Comment on the morphology of the red blood cells.
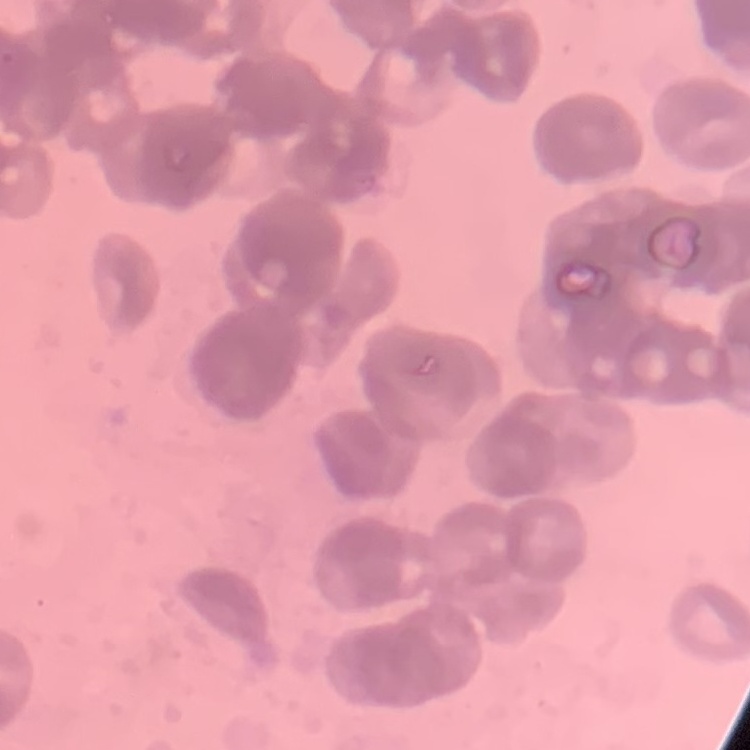

They show rouleaux formation.

stain = Field's or Giemsa
image type = square crop of a larger photomicrograph
preparation = thin blood film